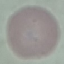
Summary:
  - Malaria status: uninfected
  - Image type: automatically extracted cell patch, resized to 64 × 64 pixels
  - Preparation: thin blood smear
  - Stain: Giemsa
  - Capture: smartphone through the microscope eyepiece